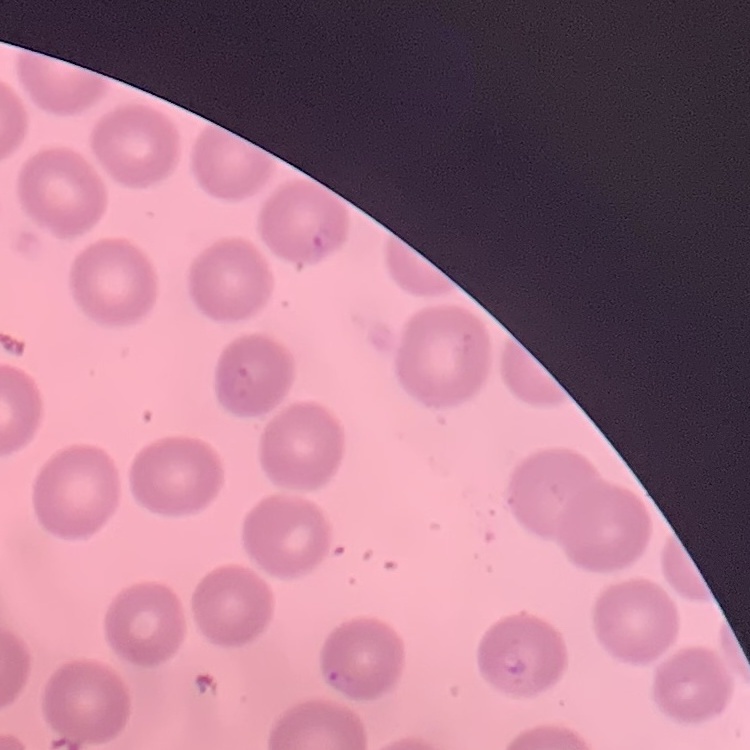
Summary:
  - Red blood cell morphology: no rouleaux formation
  - Image type: one tile cut from a larger photomicrograph
  - Preparation: thin blood smear
  - Stain: Field's or Giemsa